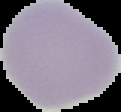

{
  "preparation": "thin blood smear",
  "malaria_status": "uninfected",
  "image_size": "121×112 pixels",
  "image_type": "segmented cell region on a black background"
}